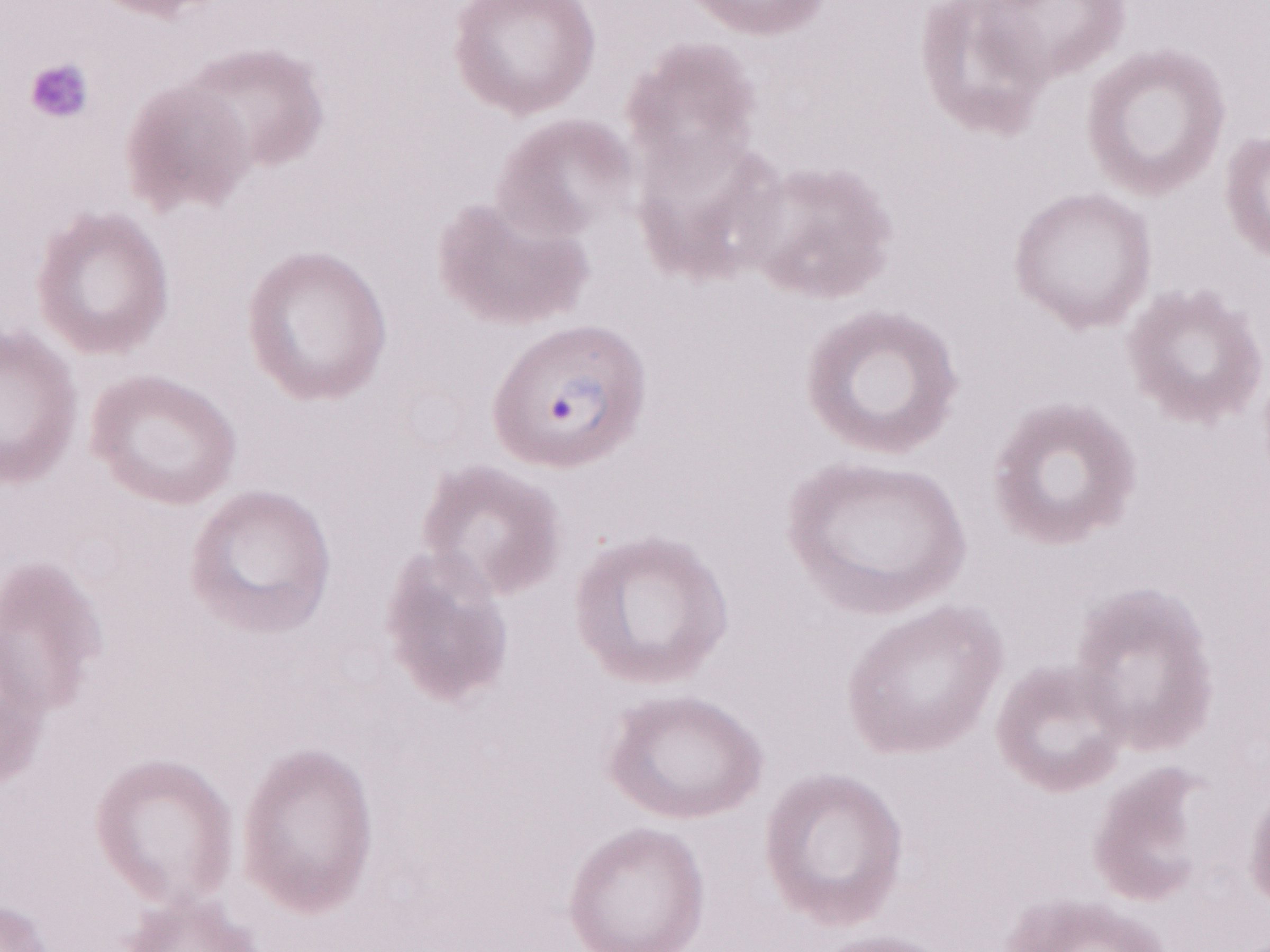 Image is 1270×952 pixels. Patient diagnosis: malaria infection. Olympus BX43 microscope, Olympus DP73 camera. May-Grünwald-Giemsa (MGG) stain. Thin blood film. 1,000x magnification. Single field of view.